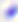

{
  "modality": "micrograph",
  "identification": "Toxoplasma gondii",
  "magnification": "400x"
}